Identify the parasite.
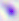

Toxoplasma gondii.

Captured at 400x magnification. Photomicrograph.